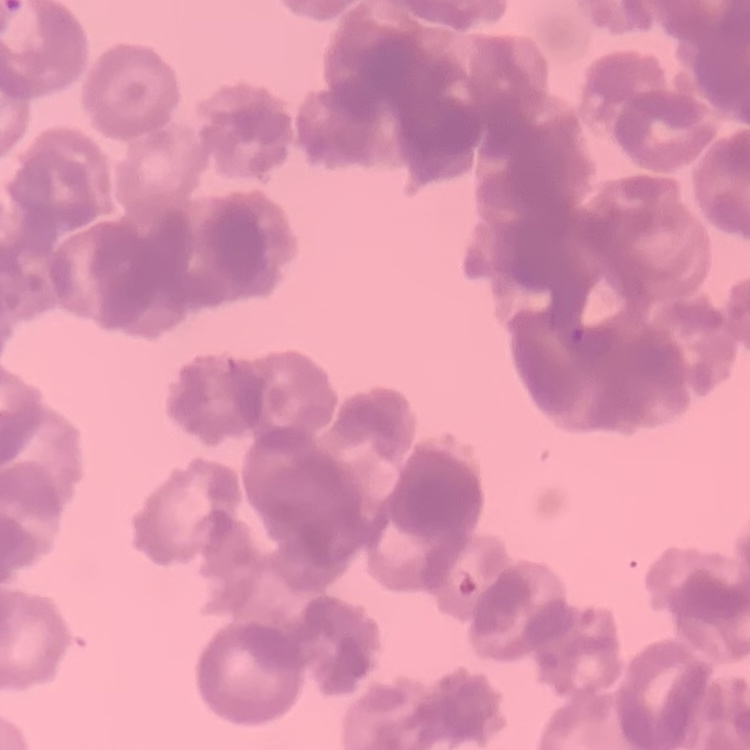
Summary:
  - Red blood cell morphology: rouleaux formation
  - Stain: Field's or Giemsa
  - Preparation: thin peripheral smear
  - Image type: one tile cut from a larger photomicrograph